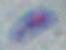
Summary:
  - Identification: Toxoplasma gondii
  - Magnification: 1000x
  - Modality: photomicrograph